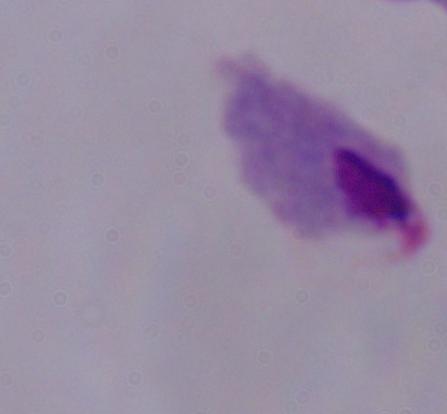

Photomicrograph. A trichomonad is seen. 1000x magnification.